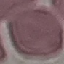
Result: no malaria parasites detected. Giemsa stain. Thin smear of blood. Photographed with a smartphone camera at the microscope eyepiece. Automatically extracted cell patch, resized to 64 × 64 pixels.